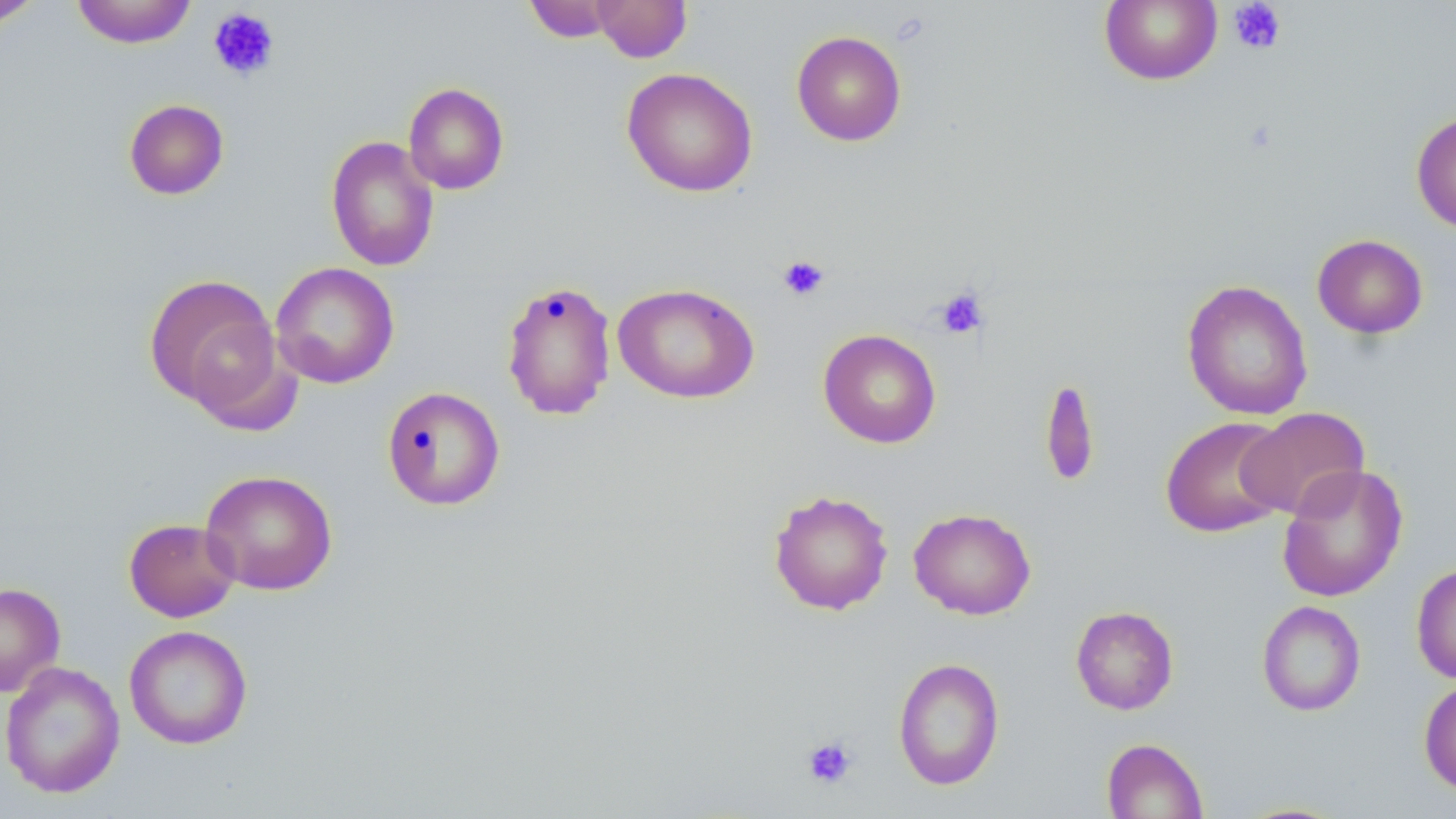 Approximate bounding boxes as [x1, y1, x2, y2] in pixels. Uninfected red blood cell locations: [0, 0, 44, 27], [71, 0, 198, 49], [524, 0, 621, 43], [591, 0, 692, 63], [1099, 0, 1222, 86], [791, 30, 907, 146], [621, 67, 758, 197], [403, 82, 510, 195], [123, 99, 229, 200], [1410, 111, 1456, 233], [325, 136, 440, 272], [1312, 233, 1428, 339], [270, 262, 400, 389], [143, 273, 284, 417], [500, 279, 617, 422], [1182, 280, 1313, 420], [612, 282, 760, 404], [818, 328, 942, 448], [1039, 376, 1101, 489], [382, 386, 506, 511], [1238, 406, 1370, 520], [1160, 416, 1291, 538], [1277, 464, 1408, 602], [200, 469, 338, 595], [768, 489, 893, 616], [908, 508, 1036, 620], [123, 518, 241, 623], [1411, 562, 1456, 684], [0, 582, 66, 697], [1257, 600, 1366, 716], [1070, 605, 1179, 715], [124, 624, 253, 750], [892, 657, 1005, 791], [1, 660, 125, 799], [1418, 677, 1456, 797], [1101, 738, 1209, 819]. Platelet locations: [1228, 0, 1287, 55], [207, 7, 280, 81], [777, 254, 830, 301], [935, 287, 989, 340], [801, 735, 858, 789]. Slide-level diagnosis: no evidence of blood parasites. Image is 1456×819 pixels. 1000x magnification. Light microscopy. May-Grünwald-Giemsa stain. Thin blood smear. Single field of view.